Comment on the morphology of the red blood cells.
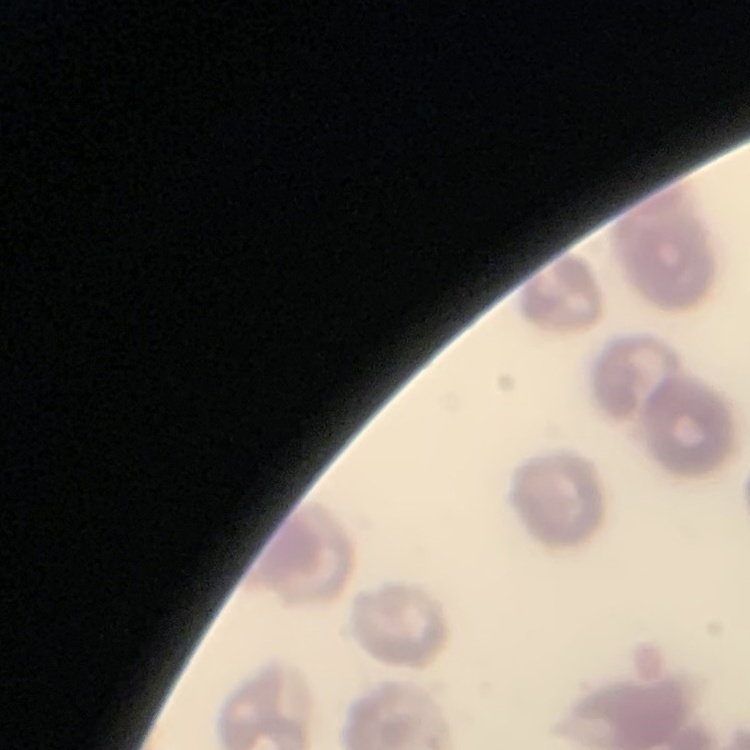

No rouleaux formation.

preparation: thin peripheral smear
image_type: one tile cut from a larger photomicrograph
stain: Field's or Giemsa